Identify the blood parasite species.
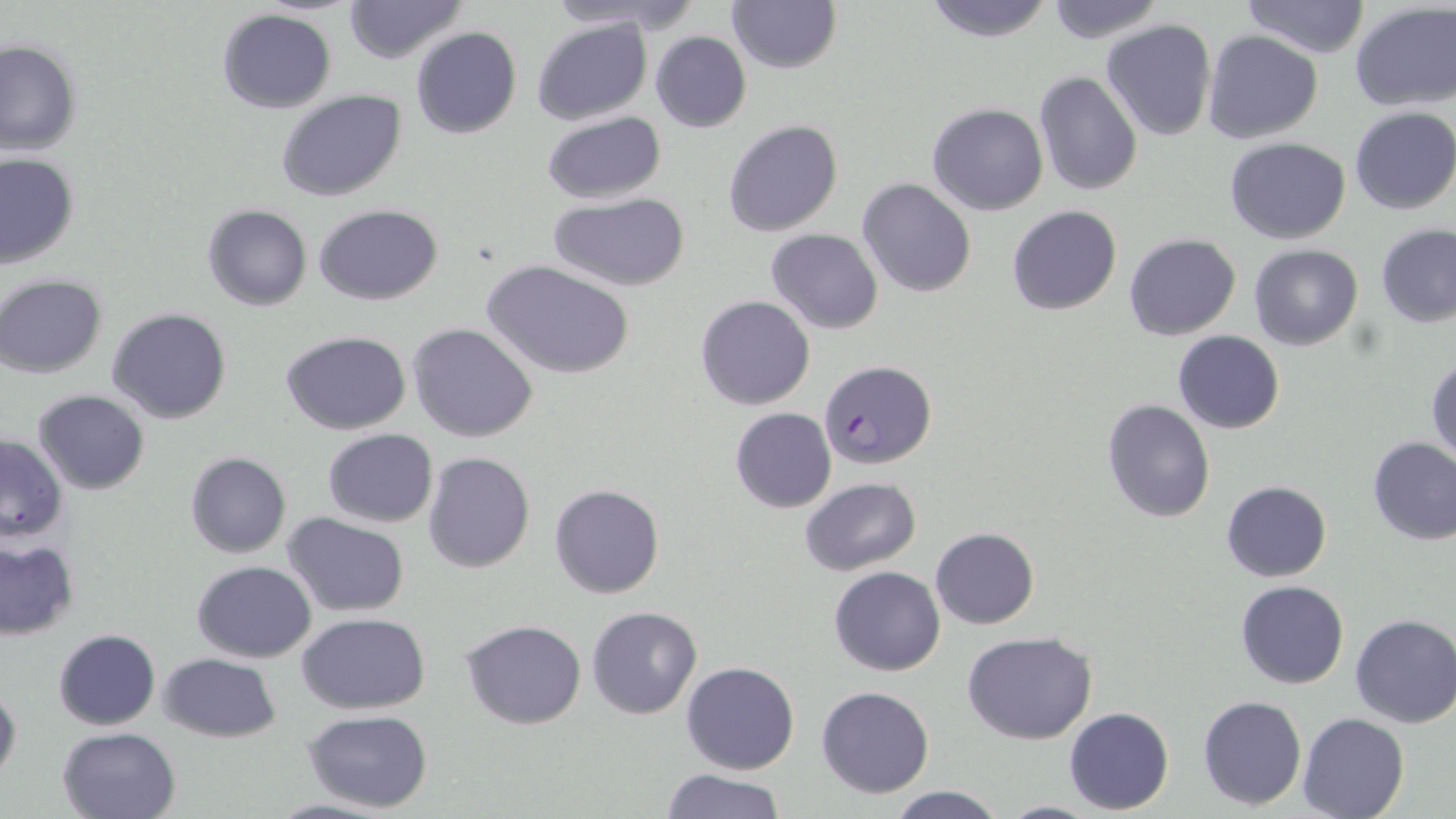

Plasmodium falciparum.

Summary:
  - Coordinate format: approximate bounding boxes as (x1,y1)-(x2,y2) corner pairs in pixels
  - Plasmodium falciparum-infected red blood cell locations: (820,360)-(937,469)
  - Uninfected red blood cell locations: (340,0)-(470,63), (543,0)-(677,29), (726,0)-(841,73), (920,0)-(1058,43), (1042,0)-(1166,43), (1240,0)-(1372,58), (1350,3)-(1456,114), (216,8)-(337,112), (533,18)-(654,125), (1101,18)-(1216,141), (411,27)-(522,140), (1204,30)-(1323,144), (650,31)-(750,133), (0,38)-(83,157), (1034,71)-(1141,195), (277,90)-(405,203), (928,102)-(1049,216), (1348,106)-(1456,215), (541,112)-(665,205), (722,119)-(844,238), (1224,137)-(1351,243), (0,153)-(80,269), (856,177)-(976,298), (547,192)-(691,291), (203,205)-(312,311), (314,205)-(441,306), (1006,205)-(1122,315), (1376,223)-(1456,327), (766,228)-(883,334), (1124,233)-(1242,341), (1249,244)-(1363,350), (483,260)-(634,379), (1,275)-(110,378), (696,295)-(816,410), (106,308)-(233,424), (407,324)-(538,443), (1172,330)-(1285,434), (282,331)-(411,435), (1427,357)-(1456,467), (32,389)-(150,494), (1102,398)-(1215,522), (730,408)-(837,513), (321,429)-(438,527), (0,436)-(67,543), (1367,437)-(1456,545), (185,452)-(291,558), (423,452)-(535,573), (799,477)-(921,576), (1222,481)-(1331,582), (549,483)-(665,599), (282,511)-(410,618), (930,528)-(1039,629), (0,539)-(79,638), (192,560)-(316,662), (828,566)-(945,676), (1235,580)-(1349,688), (586,606)-(702,719), (297,612)-(431,714), (1350,612)-(1456,727), (460,619)-(586,730), (53,629)-(159,729), (961,631)-(1099,745), (159,653)-(281,742), (681,661)-(799,774), (0,682)-(21,786), (816,685)-(936,798), (1198,695)-(1306,809), (1064,707)-(1175,814), (301,709)-(434,813), (1297,711)-(1410,818), (57,726)-(182,819), (657,768)-(787,819), (885,785)-(1008,819), (262,797)-(398,819), (994,800)-(1105,817)
  - Stain: May-Grünwald-Giemsa
  - Field of view: one of a larger specimen
  - Modality: optical microscopy
  - Magnification: 1000x
  - Preparation: thin blood smear
  - Image size: 1456×819 pixels